Locate and identify every blood parasite.
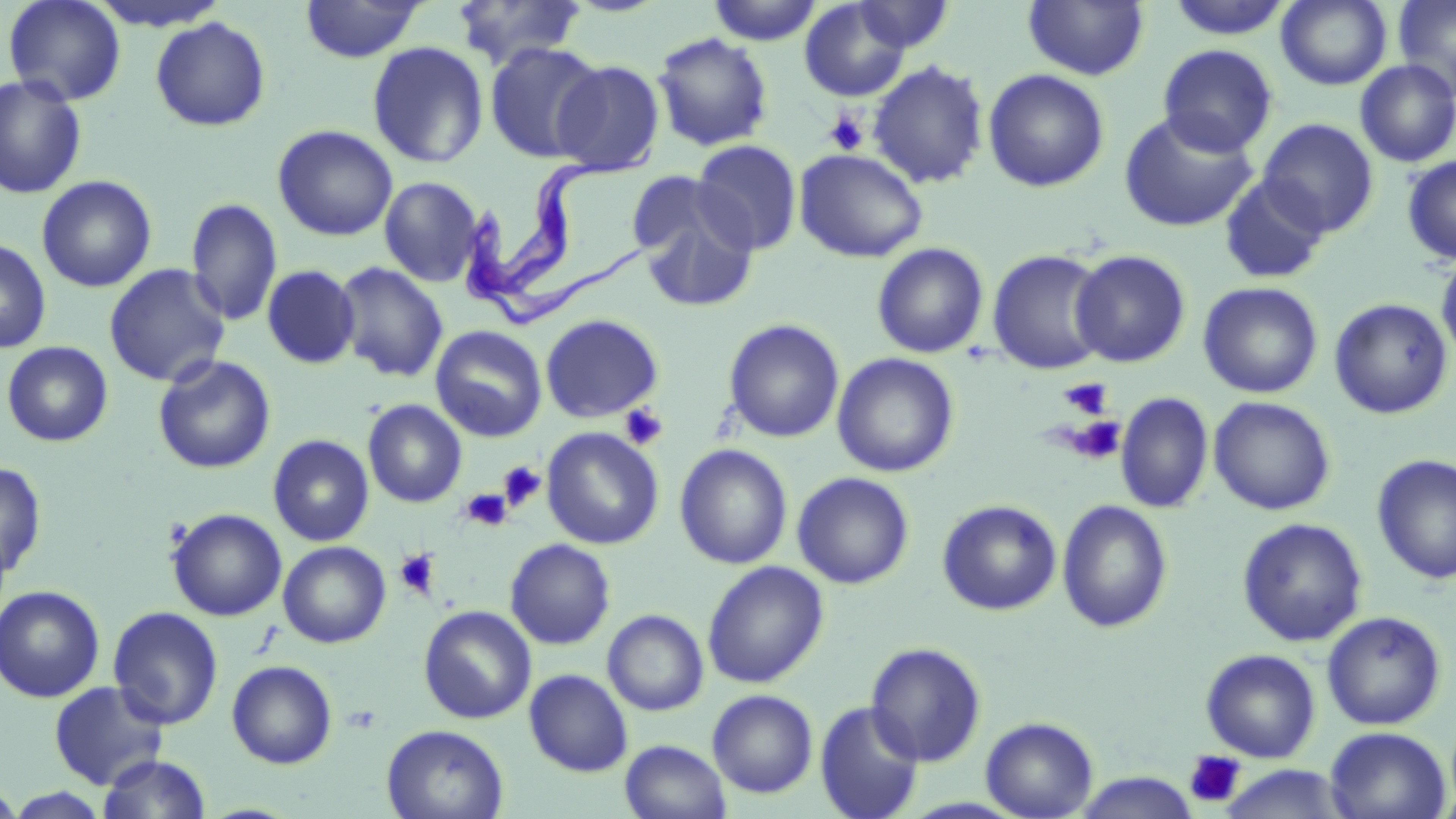
Approximate bounding boxes as (x1, y1, x2, y2) in pixels.
Trypanosoma brucei: (468, 143, 656, 334).
No Plasmodium falciparum, Plasmodium ovale, Plasmodium malariae, Plasmodium vivax, or Babesia divergens observed.

Summary:
  - Platelet locations: (824, 110, 869, 155), (1060, 377, 1113, 420), (619, 403, 669, 451), (1068, 416, 1126, 464), (497, 461, 546, 511), (460, 488, 512, 531), (395, 548, 441, 599), (1184, 751, 1245, 808)
  - Uninfected red blood cell locations: (2, 0, 127, 106), (300, 0, 425, 63), (707, 0, 822, 46), (1023, 0, 1149, 81), (1165, 0, 1295, 40), (1276, 0, 1392, 90), (1393, 0, 1456, 100), (452, 1, 588, 70), (799, 1, 912, 102), (852, 1, 954, 53), (151, 16, 271, 132), (652, 32, 773, 152), (367, 41, 489, 169), (484, 42, 606, 163), (1157, 44, 1278, 157), (551, 59, 665, 176), (867, 60, 990, 189), (1355, 60, 1456, 167), (982, 68, 1109, 192), (0, 75, 87, 200), (1119, 111, 1259, 233), (1257, 117, 1379, 237), (272, 124, 398, 242), (691, 140, 803, 256), (795, 149, 928, 263), (1402, 154, 1456, 265), (36, 175, 157, 293), (379, 176, 484, 287), (1219, 176, 1331, 286), (631, 179, 759, 313), (185, 197, 283, 327), (0, 238, 52, 354), (871, 242, 989, 359), (987, 249, 1110, 376), (1070, 250, 1191, 368), (1436, 253, 1456, 364), (334, 262, 449, 382), (103, 264, 231, 388), (262, 264, 360, 369), (1198, 282, 1323, 398), (1329, 298, 1453, 419), (540, 314, 664, 423), (722, 318, 845, 443), (430, 325, 547, 443), (1, 341, 114, 447), (832, 353, 960, 478), (153, 355, 276, 474), (1116, 392, 1213, 514), (1208, 396, 1336, 516), (363, 399, 467, 508), (541, 427, 664, 550), (268, 434, 375, 547), (674, 444, 793, 569), (1371, 454, 1456, 585), (0, 461, 47, 580), (792, 472, 915, 589), (937, 499, 1062, 615), (1057, 499, 1173, 633), (166, 508, 287, 621), (1236, 517, 1368, 647), (505, 538, 616, 649), (278, 541, 391, 648), (702, 560, 829, 688), (0, 585, 105, 703), (418, 605, 537, 724), (107, 606, 225, 730), (603, 609, 709, 716), (1321, 610, 1447, 730), (865, 641, 987, 766), (1200, 648, 1321, 762), (226, 660, 337, 769), (525, 669, 633, 777), (48, 680, 170, 789), (707, 689, 818, 798), (814, 700, 925, 819), (981, 716, 1099, 818), (382, 724, 508, 819), (1325, 726, 1451, 819), (620, 739, 731, 819), (97, 753, 212, 818), (1218, 765, 1353, 819), (1072, 771, 1199, 818), (0, 780, 24, 818), (4, 788, 113, 818)
  - Slide-level diagnosis: Trypanosoma brucei
  - Field of view: single
  - Magnification: 1000x
  - Image size: 1456×819 pixels
  - Modality: optical microscopy
  - Stain: May-Grünwald-Giemsa
  - Preparation: thin blood smear